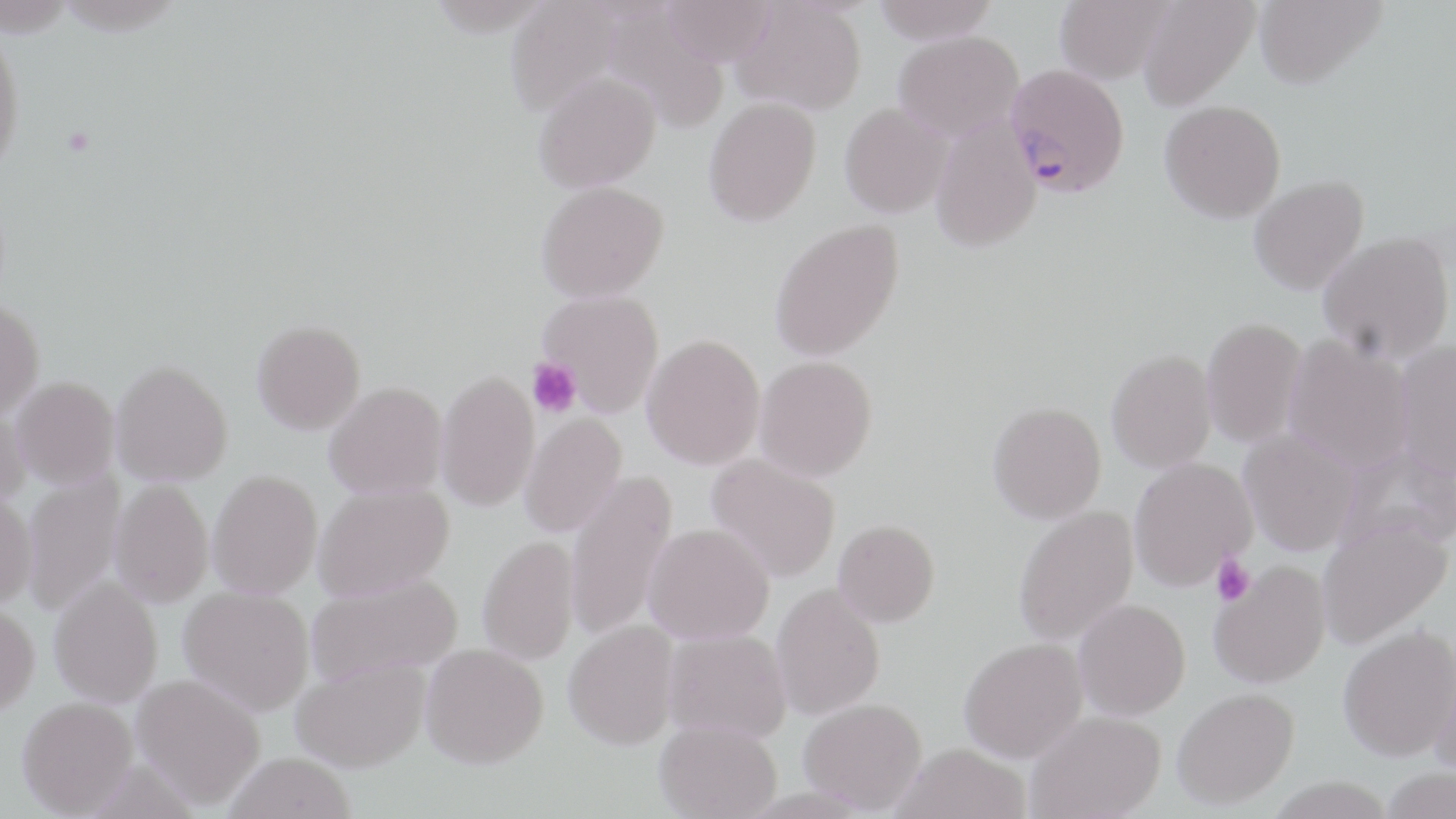

slide-level diagnosis = Plasmodium falciparum
uninfected red blood cell locations = approximate bounding boxes as named x1/y1/x2/y2 corners in pixels: (x1=505, y1=0, x2=626, y2=117), (x1=873, y1=0, x2=1000, y2=43), (x1=1054, y1=0, x2=1174, y2=83), (x1=1137, y1=0, x2=1259, y2=111), (x1=1254, y1=0, x2=1386, y2=89), (x1=659, y1=1, x2=778, y2=66), (x1=732, y1=1, x2=867, y2=116), (x1=0, y1=30, x2=25, y2=177), (x1=894, y1=30, x2=1024, y2=141), (x1=533, y1=70, x2=661, y2=192), (x1=703, y1=97, x2=821, y2=228), (x1=1160, y1=100, x2=1286, y2=223), (x1=840, y1=102, x2=952, y2=220), (x1=930, y1=119, x2=1042, y2=254), (x1=1248, y1=175, x2=1370, y2=296), (x1=537, y1=183, x2=669, y2=306), (x1=769, y1=219, x2=906, y2=364), (x1=1318, y1=232, x2=1455, y2=365), (x1=537, y1=291, x2=664, y2=419), (x1=0, y1=302, x2=45, y2=424), (x1=1201, y1=317, x2=1307, y2=448), (x1=252, y1=326, x2=366, y2=440), (x1=1284, y1=336, x2=1414, y2=474), (x1=641, y1=337, x2=765, y2=473), (x1=1395, y1=341, x2=1456, y2=482), (x1=1106, y1=350, x2=1217, y2=474), (x1=754, y1=358, x2=878, y2=485), (x1=111, y1=366, x2=233, y2=489), (x1=436, y1=374, x2=540, y2=515), (x1=11, y1=380, x2=120, y2=493), (x1=324, y1=386, x2=448, y2=501), (x1=986, y1=403, x2=1106, y2=526), (x1=0, y1=406, x2=32, y2=515), (x1=519, y1=414, x2=628, y2=540), (x1=1239, y1=429, x2=1359, y2=558), (x1=705, y1=454, x2=840, y2=584), (x1=1129, y1=458, x2=1257, y2=592), (x1=21, y1=468, x2=125, y2=615), (x1=565, y1=469, x2=678, y2=641), (x1=208, y1=474, x2=323, y2=601), (x1=110, y1=481, x2=213, y2=611), (x1=314, y1=485, x2=455, y2=605), (x1=0, y1=496, x2=37, y2=611), (x1=1014, y1=506, x2=1139, y2=647), (x1=1318, y1=518, x2=1453, y2=648), (x1=833, y1=523, x2=940, y2=631), (x1=643, y1=526, x2=774, y2=647), (x1=478, y1=538, x2=580, y2=666), (x1=1209, y1=561, x2=1331, y2=689), (x1=307, y1=574, x2=463, y2=689), (x1=49, y1=578, x2=163, y2=710), (x1=771, y1=585, x2=885, y2=721), (x1=178, y1=588, x2=314, y2=719), (x1=1074, y1=600, x2=1191, y2=721), (x1=0, y1=606, x2=40, y2=720), (x1=564, y1=623, x2=679, y2=755), (x1=1338, y1=626, x2=1456, y2=764), (x1=662, y1=631, x2=791, y2=746), (x1=960, y1=641, x2=1089, y2=766), (x1=420, y1=647, x2=549, y2=776), (x1=1430, y1=650, x2=1456, y2=782), (x1=292, y1=662, x2=430, y2=777), (x1=131, y1=676, x2=264, y2=812), (x1=1172, y1=690, x2=1300, y2=813), (x1=17, y1=700, x2=139, y2=819), (x1=799, y1=702, x2=927, y2=817), (x1=1026, y1=712, x2=1166, y2=819), (x1=654, y1=724, x2=781, y2=819), (x1=889, y1=747, x2=1031, y2=819), (x1=224, y1=756, x2=357, y2=819), (x1=1380, y1=769, x2=1456, y2=819), (x1=1265, y1=780, x2=1398, y2=819)
preparation = thin blood film
modality = optical microscopy
platelet locations = approximate bounding boxes as named x1/y1/x2/y2 corners in pixels: (x1=527, y1=358, x2=581, y2=417), (x1=1211, y1=553, x2=1255, y2=607)
field of view = one of a larger specimen
image size = 1456×819 pixels
Plasmodium falciparum-infected red blood cell locations = approximate bounding boxes as named x1/y1/x2/y2 corners in pixels: (x1=1005, y1=64, x2=1129, y2=197)
stain = May-Grünwald-Giemsa
magnification = 1000x